Locate and identify every blood parasite.
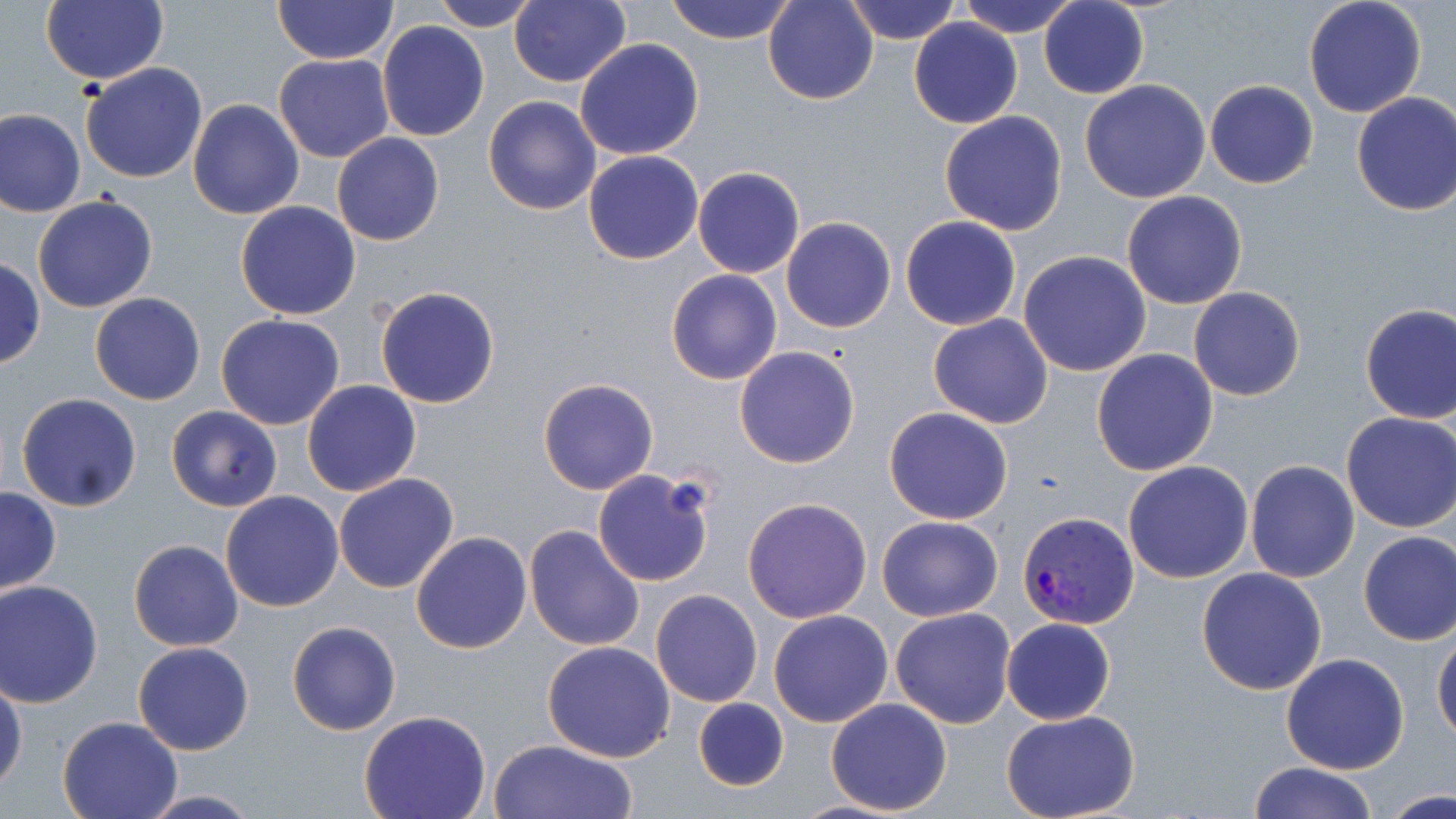
Approximate bounding boxes as (x1,y1)-(x2,y2) corner pairs in pixels.
Plasmodium vivax-infected red blood cells: (1016,509)-(1134,628).
No Plasmodium falciparum, Plasmodium ovale, Plasmodium malariae, Babesia divergens, or Trypanosoma brucei observed.

slide-level diagnosis = Plasmodium vivax
stain = May-Grünwald-Giemsa
field of view = single
image size = 1456×819 pixels
preparation = thin blood film
modality = optical microscopy
magnification = 1000x
uninfected red blood cell locations = approximate bounding boxes as (x1,y1)-(x2,y2) corner pairs in pixels: (40,0)-(168,85), (273,0)-(399,66), (431,0)-(540,31), (666,0)-(798,44), (763,0)-(879,105), (843,0)-(964,44), (956,0)-(1081,38), (1302,0)-(1428,118), (509,1)-(630,87), (1039,1)-(1149,99), (908,17)-(1024,129), (378,20)-(489,142), (575,38)-(704,161), (274,54)-(394,162), (79,63)-(208,184), (1080,79)-(1211,204), (1204,80)-(1318,189), (1351,92)-(1456,215), (482,95)-(602,215), (188,99)-(305,221), (1,108)-(85,217), (939,111)-(1068,236), (332,133)-(444,246), (583,150)-(704,265), (693,167)-(804,278), (1122,191)-(1249,310), (32,195)-(159,313), (236,201)-(362,319), (900,216)-(1020,330), (781,217)-(896,333), (1019,251)-(1152,376), (0,257)-(43,369), (665,269)-(782,385), (375,285)-(501,408), (1188,285)-(1306,401), (90,293)-(205,405), (1358,302)-(1456,423), (215,313)-(345,430), (928,313)-(1054,428), (733,346)-(859,468), (1091,348)-(1218,476), (537,378)-(659,495), (301,380)-(421,497), (17,393)-(143,511), (166,405)-(283,512), (884,407)-(1013,524), (1339,412)-(1456,532), (1122,460)-(1253,584), (1245,460)-(1361,584), (592,469)-(715,588), (332,473)-(459,594), (1,486)-(61,595), (221,491)-(344,612), (741,496)-(872,624), (876,515)-(1004,620), (523,523)-(645,652), (1357,530)-(1456,646), (411,531)-(532,654), (129,539)-(244,652), (1196,567)-(1327,695), (0,581)-(104,708), (649,589)-(763,707), (890,607)-(1017,729), (768,609)-(894,728), (1002,617)-(1115,725), (286,620)-(400,736), (1432,632)-(1456,745), (132,640)-(254,755), (541,641)-(675,762), (1280,654)-(1409,774), (0,673)-(26,795), (692,696)-(790,791), (825,697)-(953,816), (358,711)-(491,819), (1003,712)-(1139,819), (57,716)-(182,819), (488,739)-(638,819), (1248,762)-(1378,818), (1383,788)-(1452,817), (135,790)-(264,818), (785,799)-(915,819)